Identify the parasite.
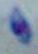

This is Toxoplasma gondii.

magnification: 1000x
modality: micrograph